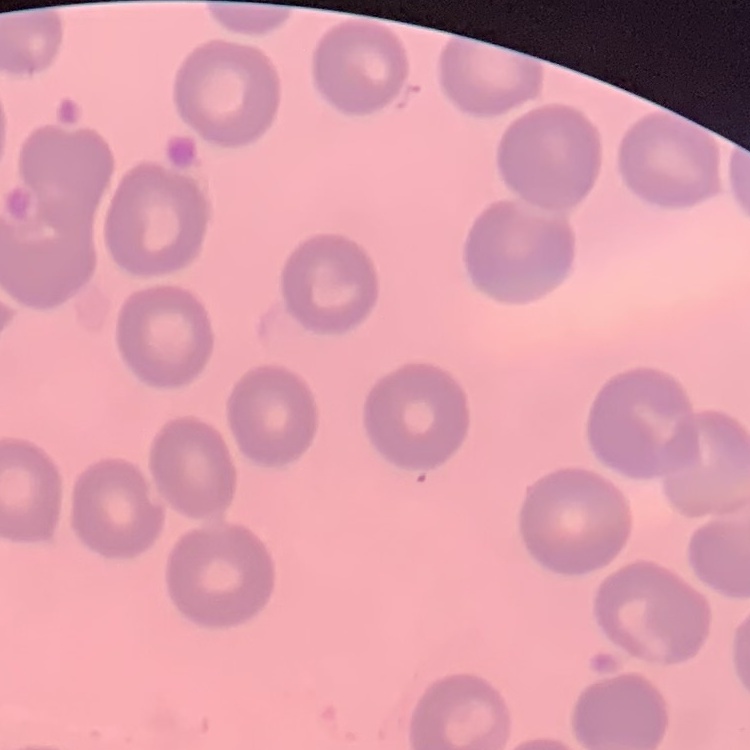
The red blood cells exhibit no rouleaux formation. Thin blood smear. One tile cut from a larger photomicrograph. Stained with either Field's or Giemsa.